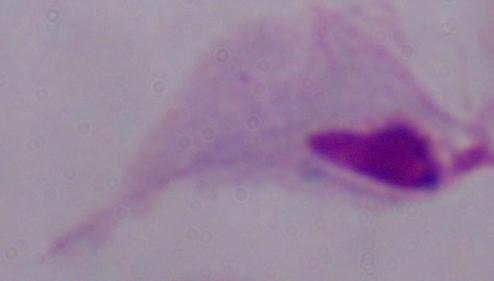

{
  "modality": "micrograph",
  "magnification": "1000x",
  "identification": "trichomonad"
}